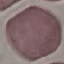
Result: negative for malaria parasites. Thin blood film. Photographed with a smartphone camera at the microscope eyepiece. Automatically extracted cell patch, resized to 64 × 64 pixels. Giemsa-stained preparation.